Describe the morphology of the red blood cells.
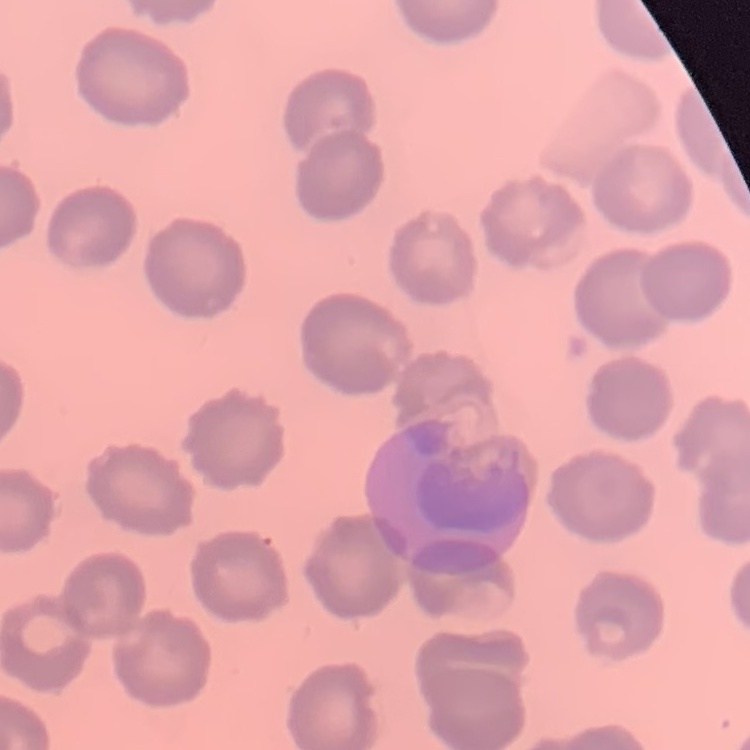

No rouleaux formation.

Square crop of a larger photomicrograph. Thin blood smear. Stained with either Field's or Giemsa.